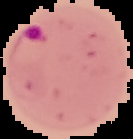
Summary:
  - Malaria status: parasitized
  - Image type: segmented cell region on a black background
  - Preparation: thin blood film
  - Image size: 133×139 pixels